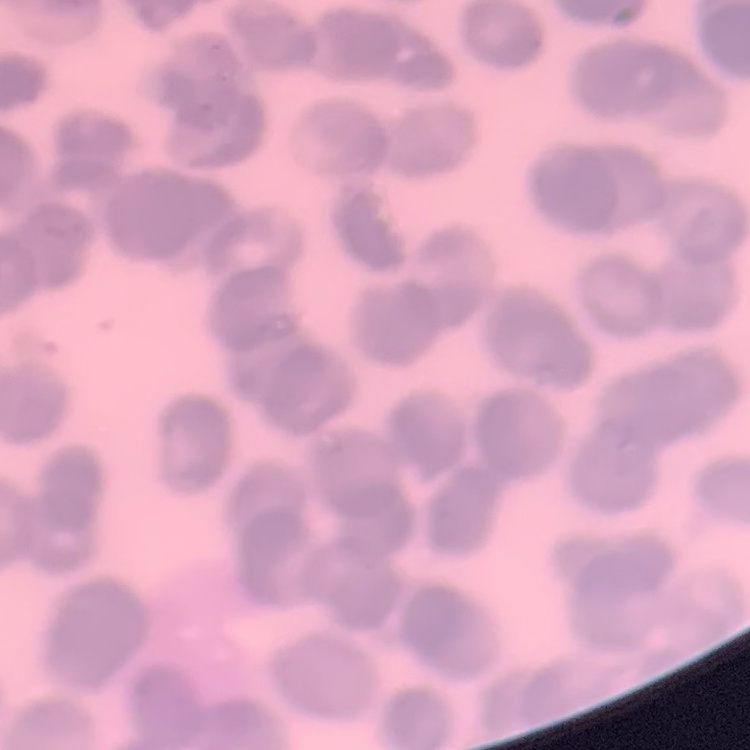
Summary:
  - Red blood cell morphology: rouleaux formation
  - Stain: Field's or Giemsa
  - Preparation: thin blood film
  - Image type: square crop of a larger photomicrograph